Assess this cell for malaria.
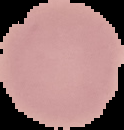

It is uninfected.

image type = segmented cell region with the area outside set to black
preparation = thin blood smear
image size = 124×130 pixels